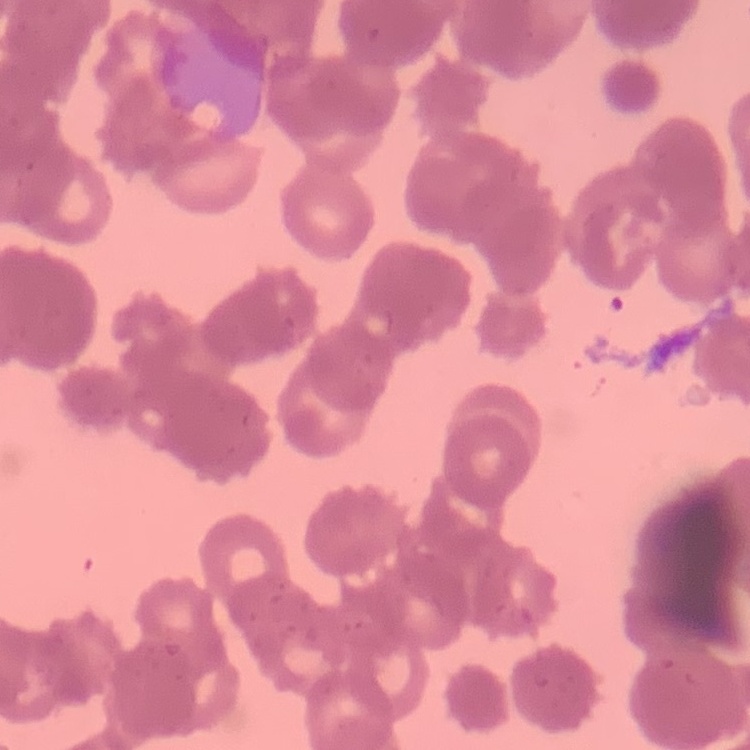

The erythrocytes show rouleaux formation. Stained with either Field's or Giemsa. One tile cut from a larger photomicrograph. Thin peripheral smear.